Assess this cell for malaria.
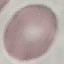

Uninfected.

Summary:
  - Preparation: thin smear
  - Image type: automatically extracted cell patch, resized to 64 × 64 pixels
  - Capture: smartphone camera at the microscope eyepiece
  - Stain: Giemsa